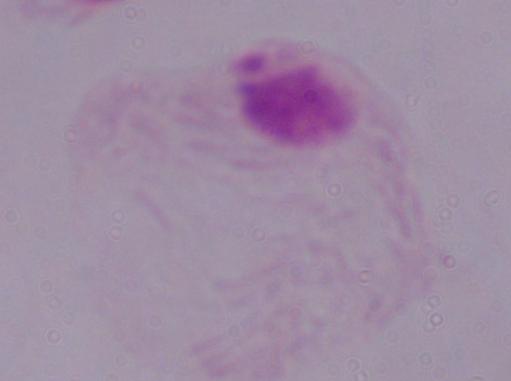

magnification = 1000x
identification = trichomonad
modality = photomicrograph